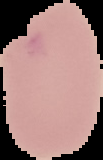 Malaria status: uninfected. Image is 103×160 pixels. The area outside the segmented cell region is set to black. From a thin blood film.